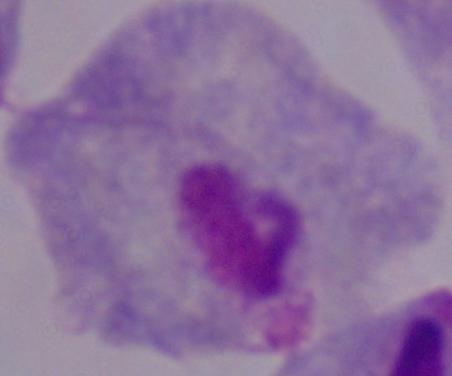

Micrograph. Captured at 1000x magnification. A trichomonad is seen.